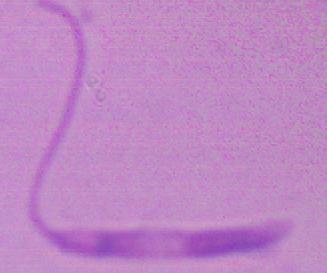
Captured at 1000x magnification. Photomicrograph. A Leishmania parasite is shown.